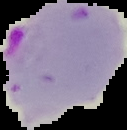
Summary:
  - Image type: segmented cell region with the area outside set to black
  - Result: Plasmodium parasites detected
  - Image size: 127×130 pixels
  - Preparation: thin blood smear